Classify this cell by malaria status.
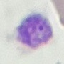
Parasitized.

Photographed with a smartphone camera at the microscope eyepiece. Cell patch, automatically extracted from a larger field of view and resized to 64 × 64 pixels. Giemsa stain. Thin smear of blood.